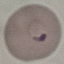

malaria status = parasitized
preparation = thin blood smear
capture = smartphone through the microscope eyepiece
image type = automatically extracted cell patch, resized to 64 × 64 pixels
stain = Giemsa